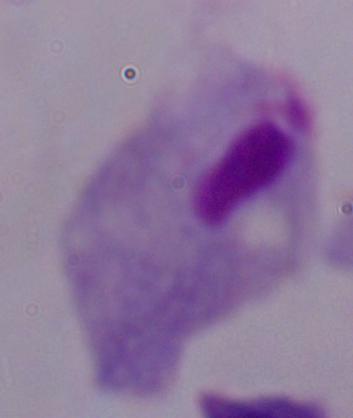

{
  "magnification": "1000x",
  "identification": "trichomonad",
  "modality": "photomicrograph"
}